Name the cell type shown.
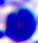

A leukocyte.

magnification = 400x
modality = micrograph